Name the parasite shown.
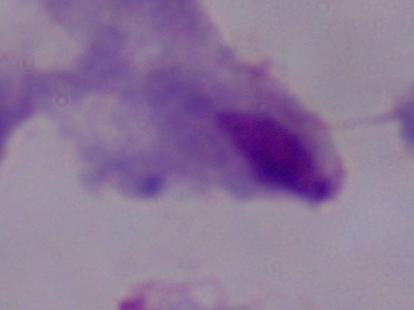
A trichomonad.

Summary:
  - Modality: photomicrograph
  - Magnification: 1000x